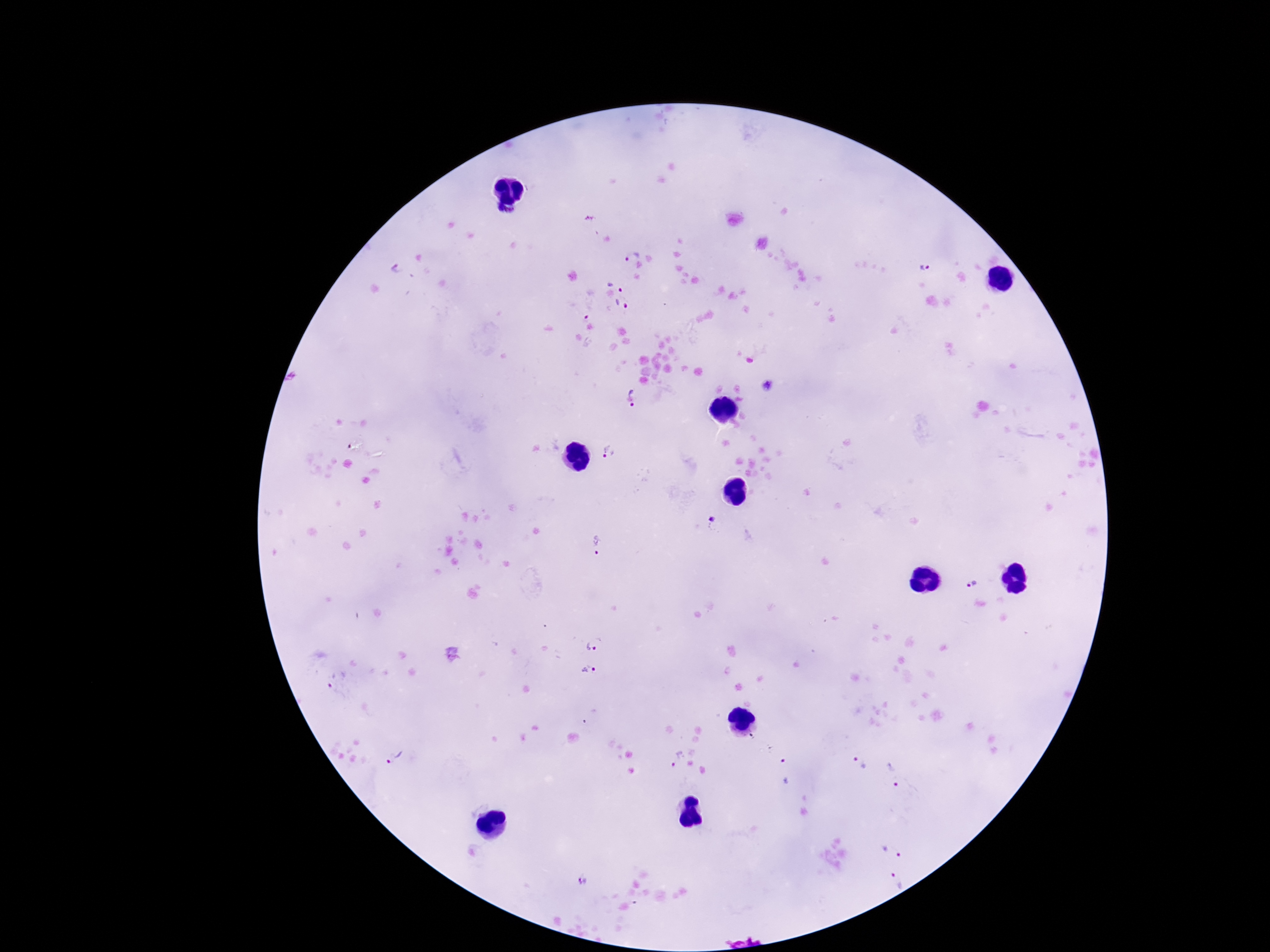
{
  "magnification": "100x",
  "plasmodium_parasite_locations": "approximate centers as {x, y} in pixels: {504, 218}, {630, 256}, {926, 267}, {396, 269}, {618, 282}, {621, 303}, {589, 310}, {768, 383}, {631, 395}, {609, 451}, {595, 543}, {968, 584}, {595, 639}, {591, 674}, {336, 678}, {395, 756}, {676, 757}, {859, 763}, {784, 770}, {894, 774}, {897, 841}, {893, 876}, {581, 879}",
  "patient_malaria_status": "infected",
  "capture": "smartphone camera through the microscope eyepiece",
  "stain": "Giemsa",
  "image_size": "1270×952 pixels",
  "preparation": "thick blood smear",
  "field_of_view": "one from this slide"
}